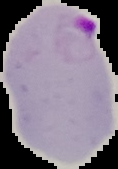
Summary:
  - Image size: 118×169 pixels
  - Malaria status: parasitized
  - Image type: segmented cell region on a black background
  - Preparation: thin blood smear